Classify this cell by malaria status.
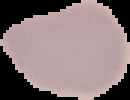
Uninfected.

Summary:
  - Image type: segmented cell region with the area outside set to black
  - Image size: 130×100 pixels
  - Preparation: thin blood smear